Locate and identify every blood parasite.
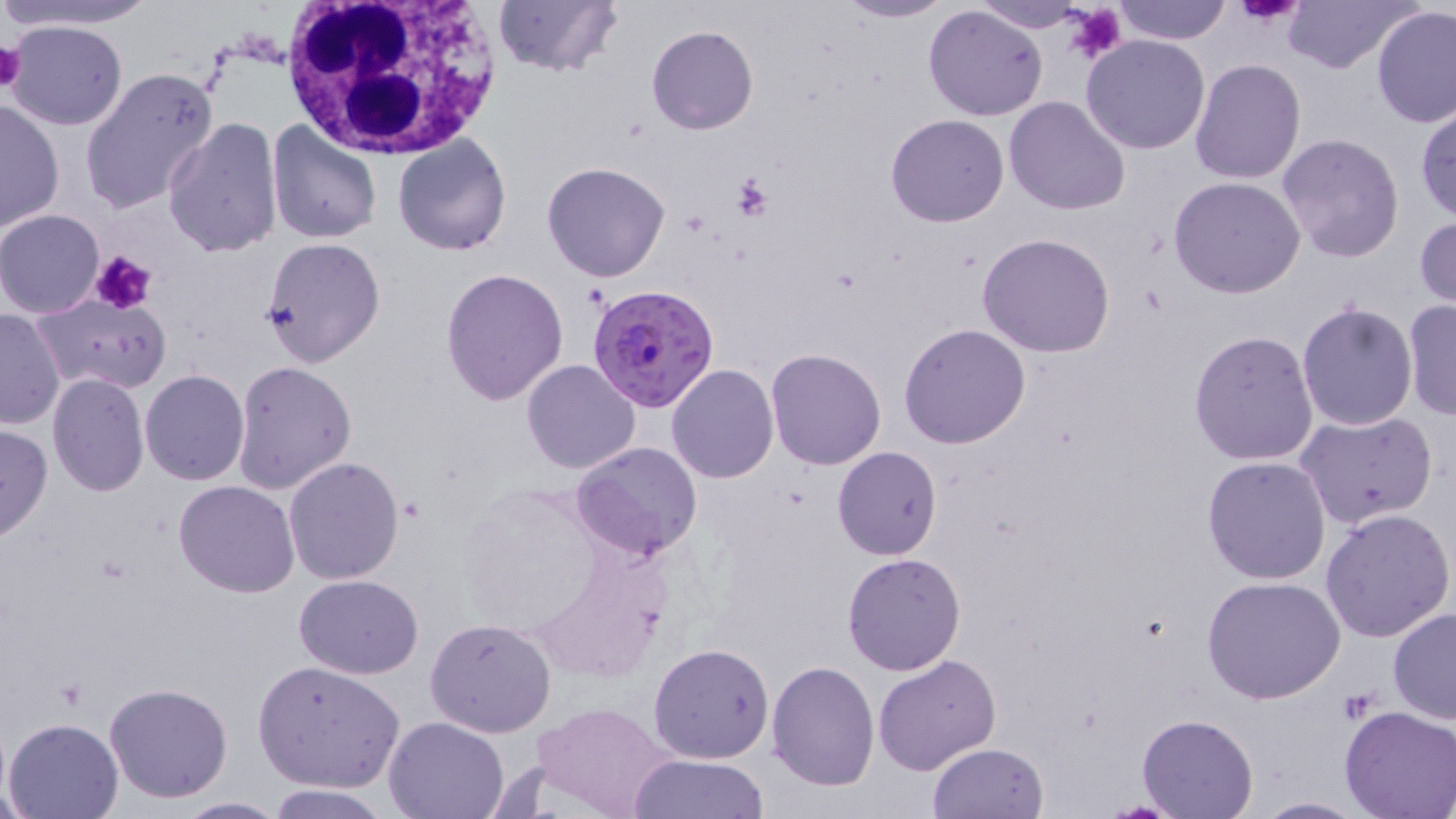

Approximate bounding boxes as (x1, y1, x2, y2) in pixels.
Plasmodium falciparum-infected red blood cells: (585, 284, 717, 412).
No Plasmodium ovale, Plasmodium malariae, Plasmodium vivax, Babesia divergens, or Trypanosoma brucei observed.

slide-level diagnosis = Plasmodium falciparum
preparation = thin blood smear
uninfected red blood cell locations = approximate bounding boxes as (x1, y1, x2, y2) in pixels: (4, 0, 160, 30), (491, 0, 622, 79), (970, 0, 1097, 34), (1113, 0, 1233, 44), (1284, 0, 1419, 72), (833, 1, 955, 24), (922, 5, 1049, 121), (1372, 7, 1456, 128), (4, 19, 128, 131), (646, 25, 758, 134), (1082, 35, 1211, 154), (1190, 59, 1307, 185), (80, 69, 218, 214), (1004, 96, 1131, 217), (1, 97, 63, 234), (1415, 101, 1456, 224), (884, 114, 1010, 226), (163, 117, 284, 257), (265, 120, 381, 243), (392, 133, 514, 256), (1274, 133, 1405, 264), (542, 162, 671, 282), (1169, 177, 1305, 298), (0, 209, 104, 318), (1415, 215, 1456, 312), (977, 233, 1116, 357), (260, 237, 386, 368), (440, 268, 568, 407), (34, 292, 171, 393), (1401, 300, 1456, 420), (1296, 301, 1419, 431), (0, 307, 66, 428), (900, 323, 1031, 448), (1189, 329, 1320, 467), (764, 348, 886, 470), (521, 360, 641, 474), (231, 361, 357, 494), (667, 364, 778, 482), (139, 370, 250, 486), (46, 372, 150, 497), (1296, 410, 1437, 531), (0, 423, 53, 542), (572, 440, 703, 560), (832, 446, 943, 561), (284, 456, 404, 584), (1202, 456, 1332, 585), (174, 480, 301, 598), (454, 484, 618, 644), (1321, 509, 1454, 644), (842, 553, 967, 674), (294, 573, 423, 676), (1202, 576, 1346, 705), (1388, 606, 1456, 726), (426, 617, 556, 738), (649, 643, 774, 762), (874, 652, 1000, 775), (647, 655, 880, 781), (767, 660, 881, 791), (254, 661, 406, 792), (104, 682, 234, 803), (534, 700, 680, 819), (1336, 707, 1456, 818), (1135, 714, 1258, 818), (382, 716, 511, 819), (3, 717, 124, 819), (926, 742, 1049, 818), (630, 754, 771, 817), (265, 784, 391, 818), (171, 795, 288, 817), (1247, 796, 1368, 818)
image size = 1456×819 pixels
platelet locations = approximate bounding boxes as (x1, y1, x2, y2) in pixels: (1237, 0, 1305, 27), (1062, 1, 1127, 66), (0, 39, 27, 93), (728, 177, 772, 220), (92, 249, 157, 315), (1337, 688, 1380, 724)
field of view = single
modality = optical microscopy
stain = May-Grünwald-Giemsa
magnification = 1000x
white blood cell locations = approximate bounding boxes as (x1, y1, x2, y2) in pixels: (273, 0, 508, 162)